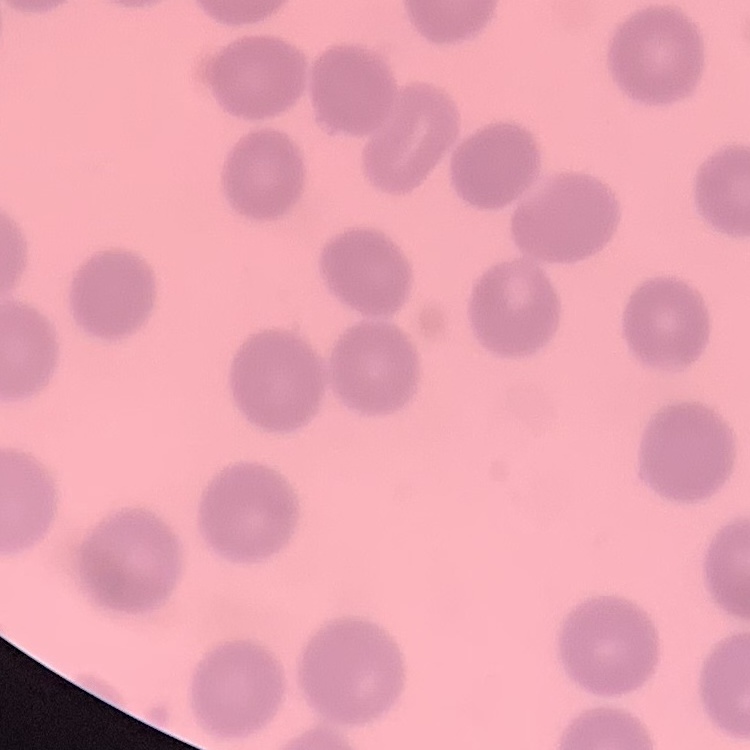
The erythrocytes show no rouleaux formation. Square crop of a larger photomicrograph. Field's or Giemsa stain. Thin blood film.